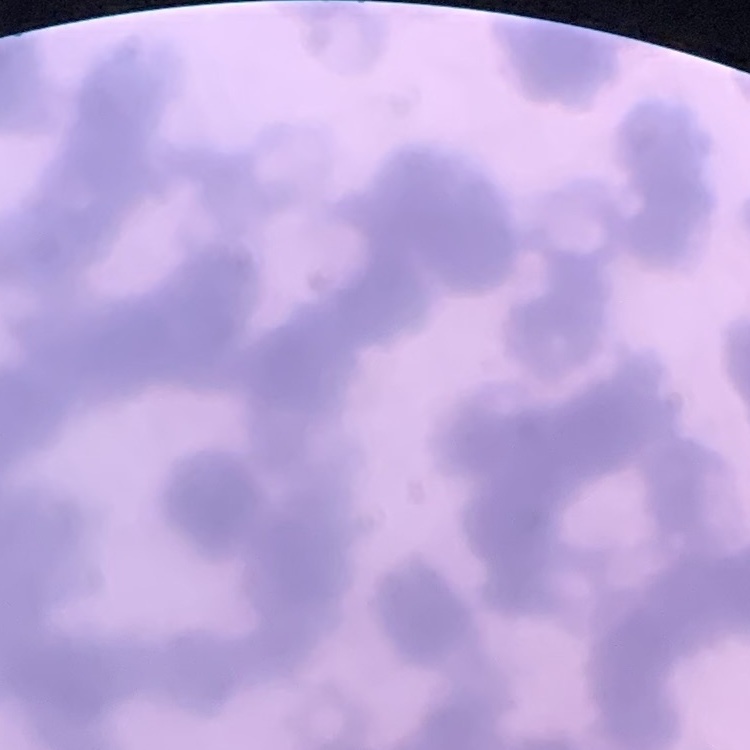 The erythrocytes exhibit rouleaux formation. Square crop of a larger photomicrograph. Thin blood smear. Field's or Giemsa stain.